Describe the morphology of the red blood cells.
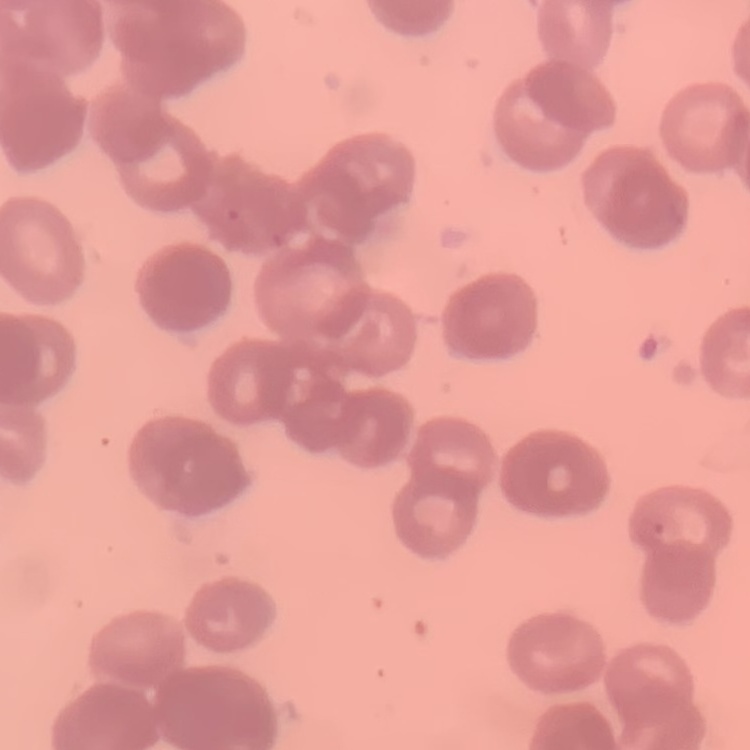

Rouleaux formation.

One tile cut from a larger photomicrograph. Thin blood film. Stained with either Field's or Giemsa.